Locate every blood parasite and identify its species.
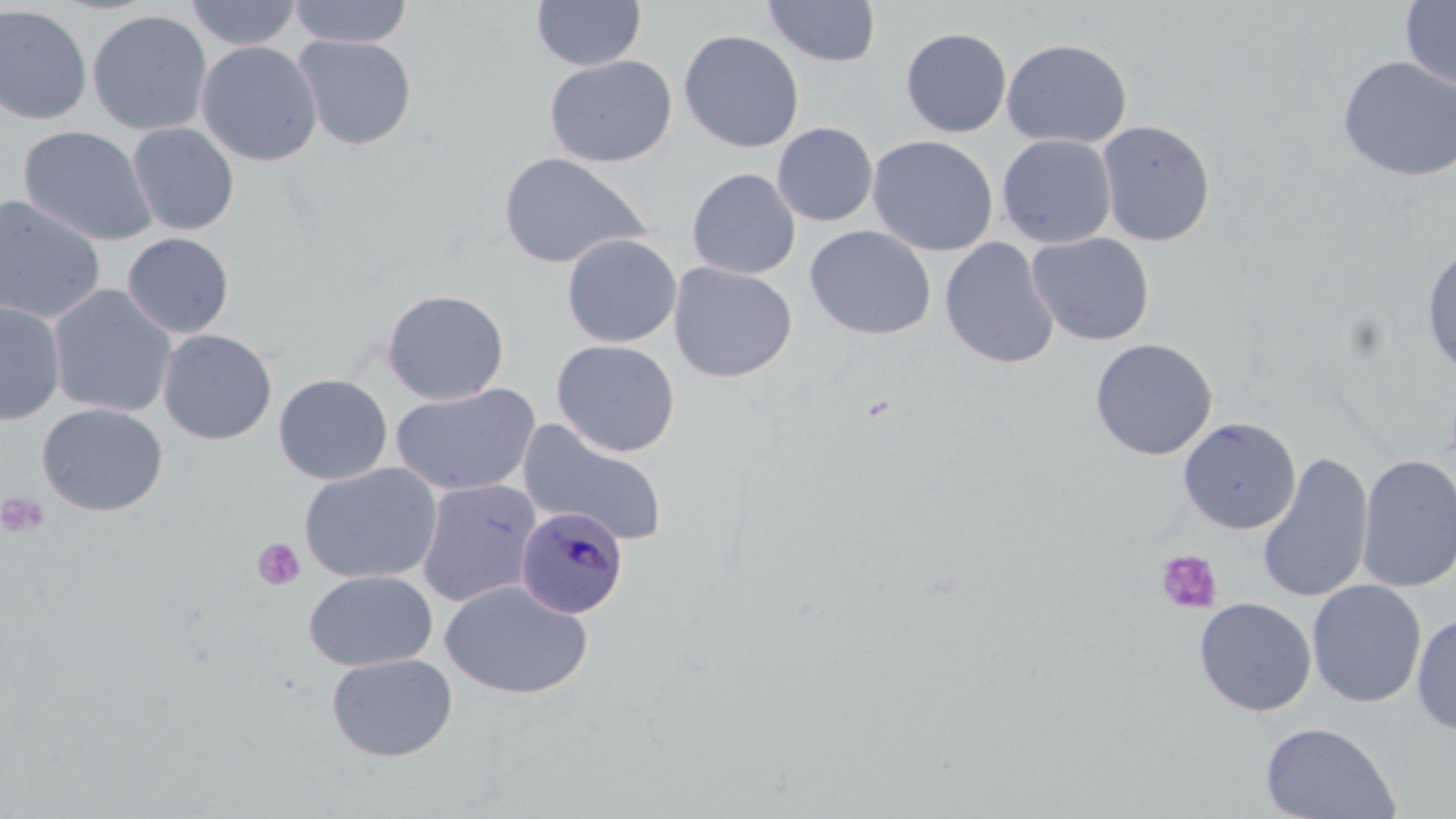
Approximate bounding boxes as (x1,y1)-(x2,y2) corner pairs in pixels.
Plasmodium malariae-infected red blood cells: (516,505)-(629,618).
No Plasmodium falciparum, Plasmodium ovale, Plasmodium vivax, Babesia divergens, or Trypanosoma brucei observed.

Platelet locations: (1,491)-(50,538), (251,537)-(306,592), (1155,549)-(1223,614). Uninfected red blood cell locations: (184,0)-(302,50), (287,0)-(414,48), (531,0)-(646,71), (1400,0)-(1456,92), (763,1)-(882,68), (0,5)-(92,125), (86,10)-(213,136), (900,27)-(1012,137), (678,29)-(804,153), (292,35)-(417,150), (1001,38)-(1132,149), (196,41)-(323,167), (544,55)-(677,168), (1336,56)-(1456,183), (1096,119)-(1216,246), (127,122)-(239,236), (771,122)-(878,226), (18,126)-(157,247), (996,133)-(1117,248), (866,135)-(998,256), (498,151)-(651,269), (687,167)-(801,279), (0,195)-(106,324), (804,225)-(937,340), (121,232)-(235,338), (1026,232)-(1155,346), (561,233)-(682,347), (939,237)-(1060,370), (1421,241)-(1455,378), (668,262)-(797,383), (47,285)-(176,418), (381,288)-(509,405), (0,299)-(66,425), (157,328)-(277,445), (1090,338)-(1218,461), (551,339)-(681,457), (273,374)-(393,485), (391,383)-(541,496), (37,403)-(168,517), (1177,417)-(1301,534), (517,419)-(671,549), (1256,452)-(1374,604), (1355,454)-(1456,594), (299,462)-(443,584), (416,478)-(542,607), (303,570)-(437,671), (1306,580)-(1427,708), (439,581)-(594,700), (1194,597)-(1316,716), (1411,613)-(1456,736), (326,653)-(458,762), (1260,722)-(1400,819). Slide-level diagnosis: Plasmodium malariae. Captured at 1000x magnification. Optical microscopy. One field of a larger specimen. May-Grünwald-Giemsa stain. Image is 1456×819 pixels. Thin blood film.